Assess the morphology of the erythrocytes.
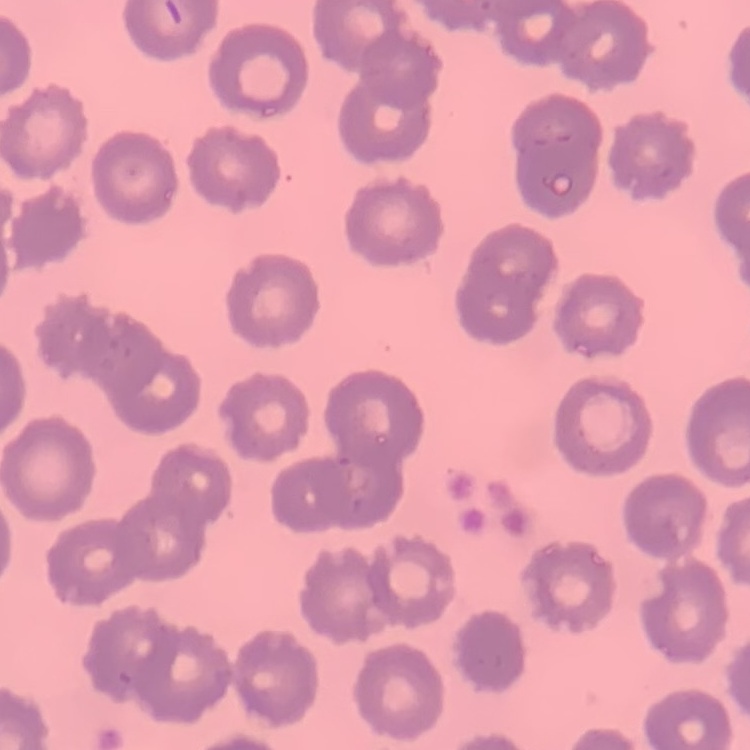
They show no rouleaux formation.

stain = Field's or Giemsa
image type = one tile cut from a larger photomicrograph
preparation = thin blood film